Locate every blood parasite and identify its species.
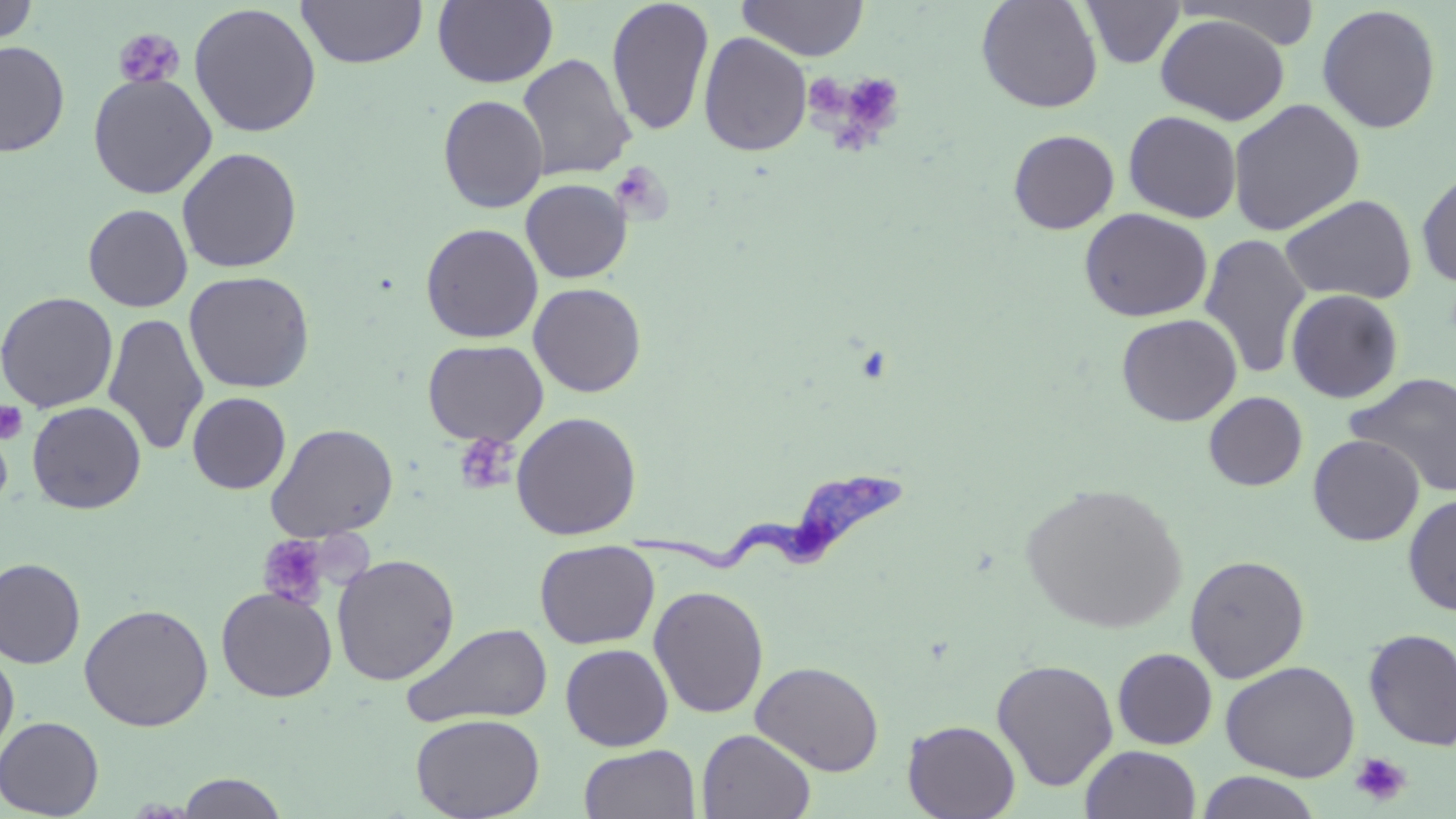

Approximate bounding boxes as (x1, y1, x2, y2) in pixels.
Trypanosoma brucei: (624, 473, 914, 574).
No Plasmodium falciparum, Plasmodium ovale, Plasmodium malariae, Plasmodium vivax, or Babesia divergens observed.

Summary:
  - Platelet locations: (113, 28, 186, 90), (836, 72, 908, 145), (610, 162, 673, 224), (0, 401, 28, 445), (460, 434, 517, 490), (256, 535, 331, 610), (1349, 752, 1412, 806)
  - Uninfected red blood cell locations: (296, 0, 428, 69), (432, 0, 558, 88), (736, 0, 869, 62), (976, 0, 1103, 113), (1081, 0, 1185, 69), (1175, 0, 1324, 50), (1, 1, 38, 46), (606, 1, 715, 136), (188, 3, 322, 138), (1317, 4, 1442, 133), (1155, 13, 1289, 125), (699, 32, 813, 157), (0, 41, 70, 156), (517, 53, 636, 181), (88, 73, 217, 199), (437, 94, 549, 213), (1227, 98, 1366, 236), (1123, 110, 1242, 223), (1007, 129, 1120, 234), (177, 147, 302, 273), (1416, 169, 1456, 289), (520, 179, 632, 283), (1279, 194, 1418, 304), (83, 203, 192, 312), (1078, 207, 1213, 322), (420, 223, 543, 343), (1198, 232, 1313, 379), (184, 270, 316, 393), (528, 282, 646, 397), (1285, 288, 1404, 403), (0, 291, 118, 413), (103, 312, 209, 456), (1116, 313, 1242, 426), (421, 339, 548, 446), (1345, 371, 1456, 497), (1203, 391, 1308, 491), (187, 392, 291, 494), (27, 401, 147, 514), (510, 411, 642, 540), (267, 423, 399, 541), (1308, 434, 1424, 545), (1019, 482, 1188, 635), (1403, 492, 1456, 616), (534, 540, 660, 649), (331, 553, 461, 686), (1184, 554, 1310, 683), (0, 558, 85, 669), (648, 585, 769, 719), (216, 586, 337, 702), (79, 603, 214, 731), (401, 622, 554, 728), (1362, 628, 1456, 750), (560, 643, 673, 751), (0, 646, 19, 760), (1112, 648, 1217, 749), (992, 658, 1119, 791), (750, 660, 884, 776), (1220, 660, 1360, 782), (410, 712, 544, 819), (0, 716, 105, 818), (902, 719, 1020, 819), (697, 728, 816, 819), (579, 744, 701, 819), (1081, 745, 1202, 819), (1196, 771, 1321, 819), (176, 772, 289, 818)
  - Slide-level diagnosis: Trypanosoma brucei
  - Preparation: thin blood smear
  - Image size: 1456×819 pixels
  - Modality: light microscopy
  - Magnification: 1000x
  - Field of view: one of a larger specimen
  - Stain: May-Grünwald-Giemsa